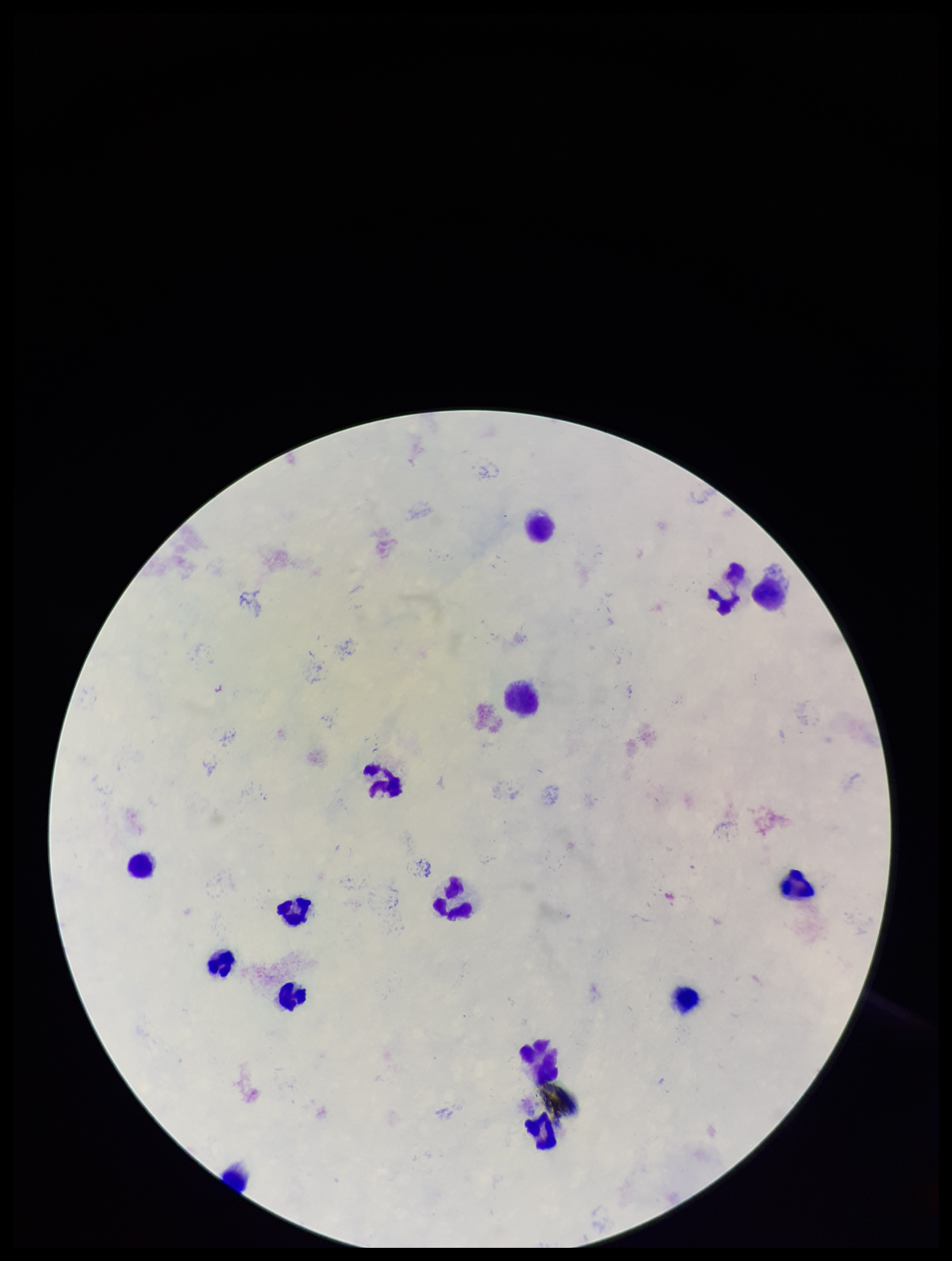

Summary:
  - Leukocyte count: 15
  - Plasmodium parasites: none identified
  - Patient malaria status: negative
  - Stain: Giemsa
  - Image size: 952×1261 pixels
  - Field of view: one from this slide
  - Capture: smartphone photograph through the microscope eyepiece
  - Preparation: thick smear
  - Parasite count: 0